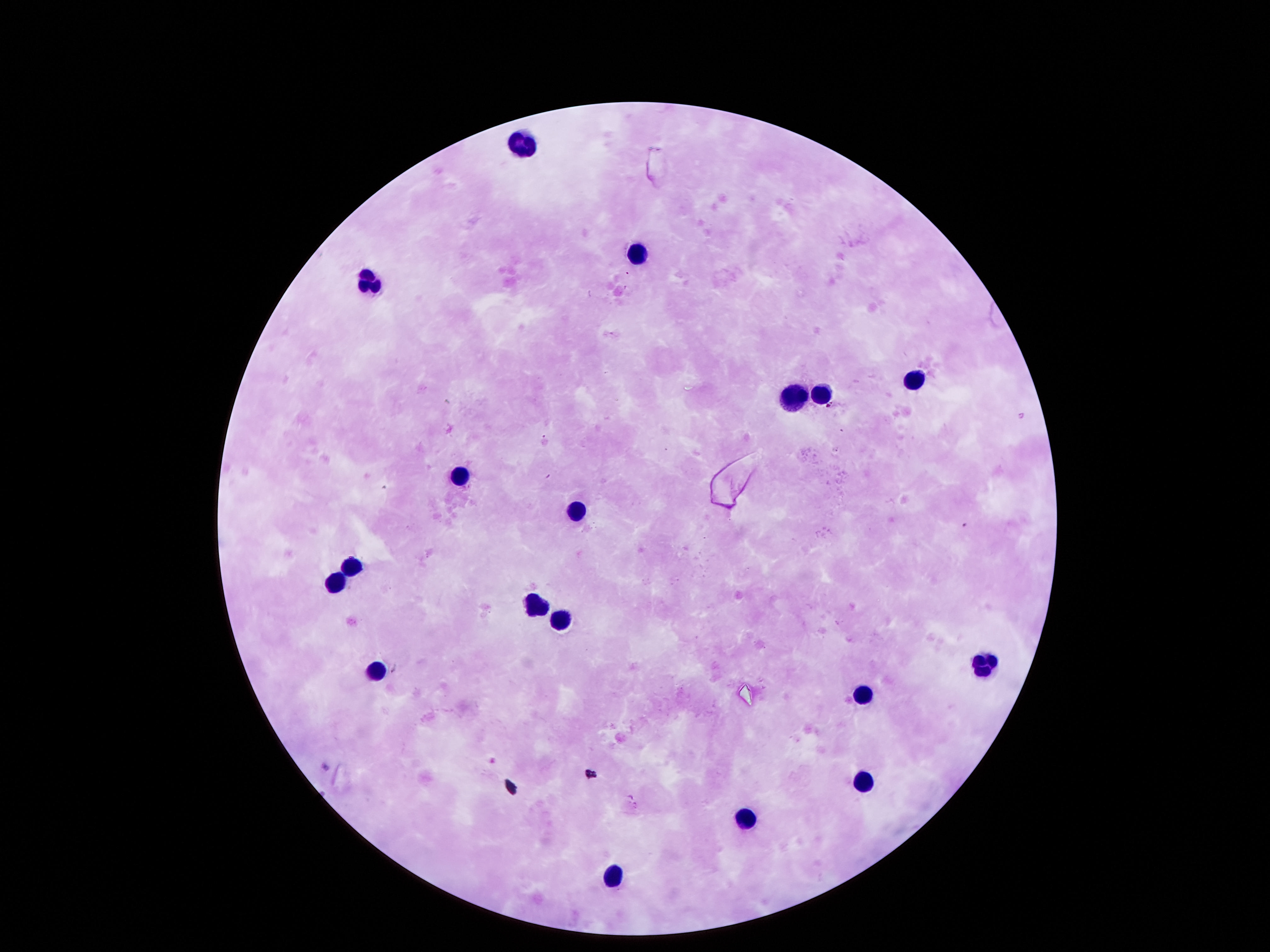

magnification = 100x
capture = smartphone camera through the microscope eyepiece
preparation = thick blood film
leukocyte locations = approximate centers as [x, y] in pixels: [522, 140], [640, 247], [366, 284], [911, 374], [795, 396], [823, 396], [459, 473], [575, 511], [354, 561], [332, 589], [537, 603], [559, 619], [985, 663], [372, 670], [861, 698], [864, 782], [743, 819], [612, 877]
image size = 1270×952 pixels
field of view = one from this slide
stain = Giemsa
patient malaria status = not infected